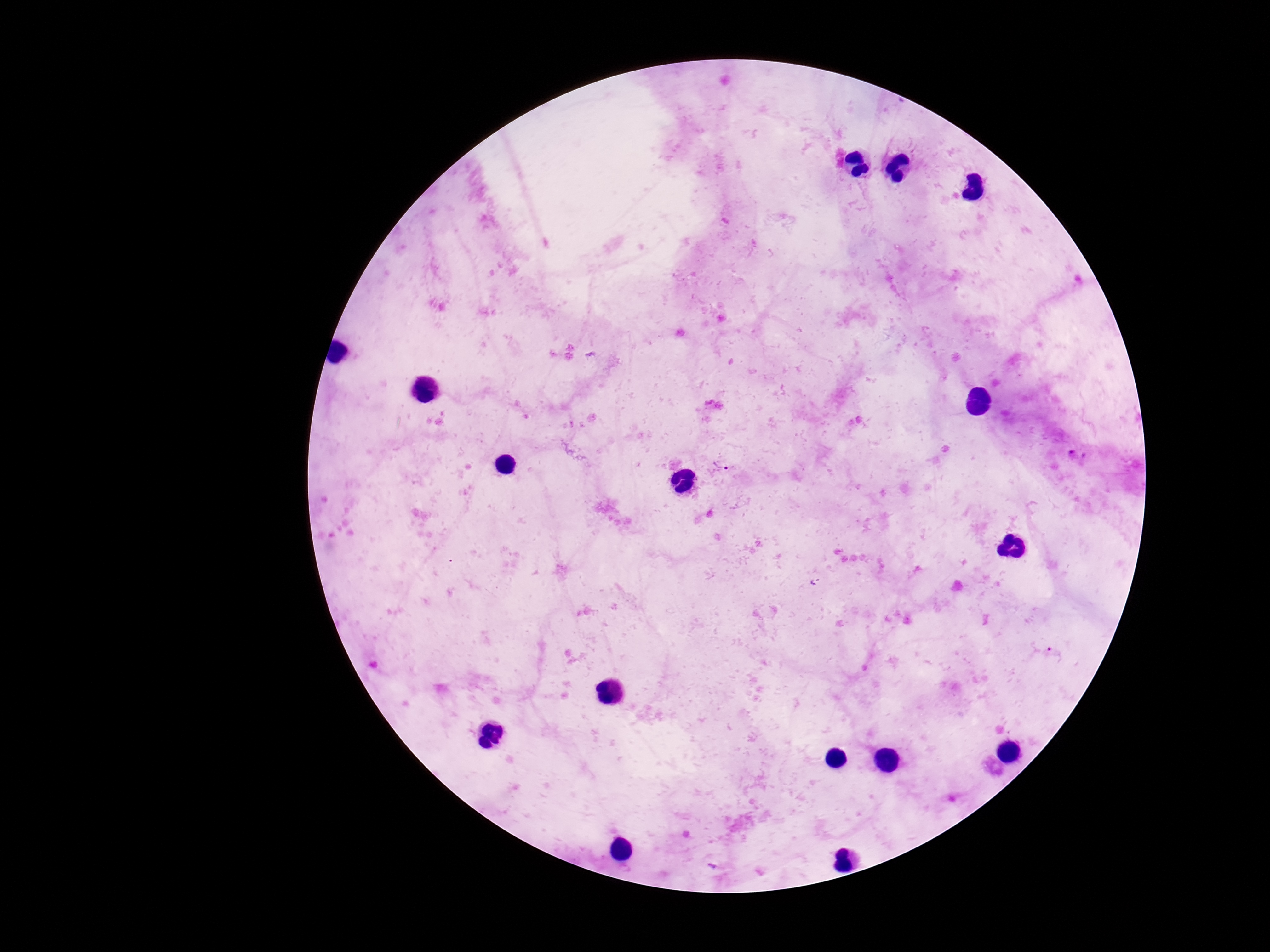

field of view = single
magnification = 100x
Plasmodium parasite locations = approximate object centers, in pixels from the top-left corner: (x=722, y=465)
preparation = thick blood smear
capture = smartphone camera through the microscope eyepiece
patient malaria status = positive
image size = 1270×952 pixels
stain = Giemsa